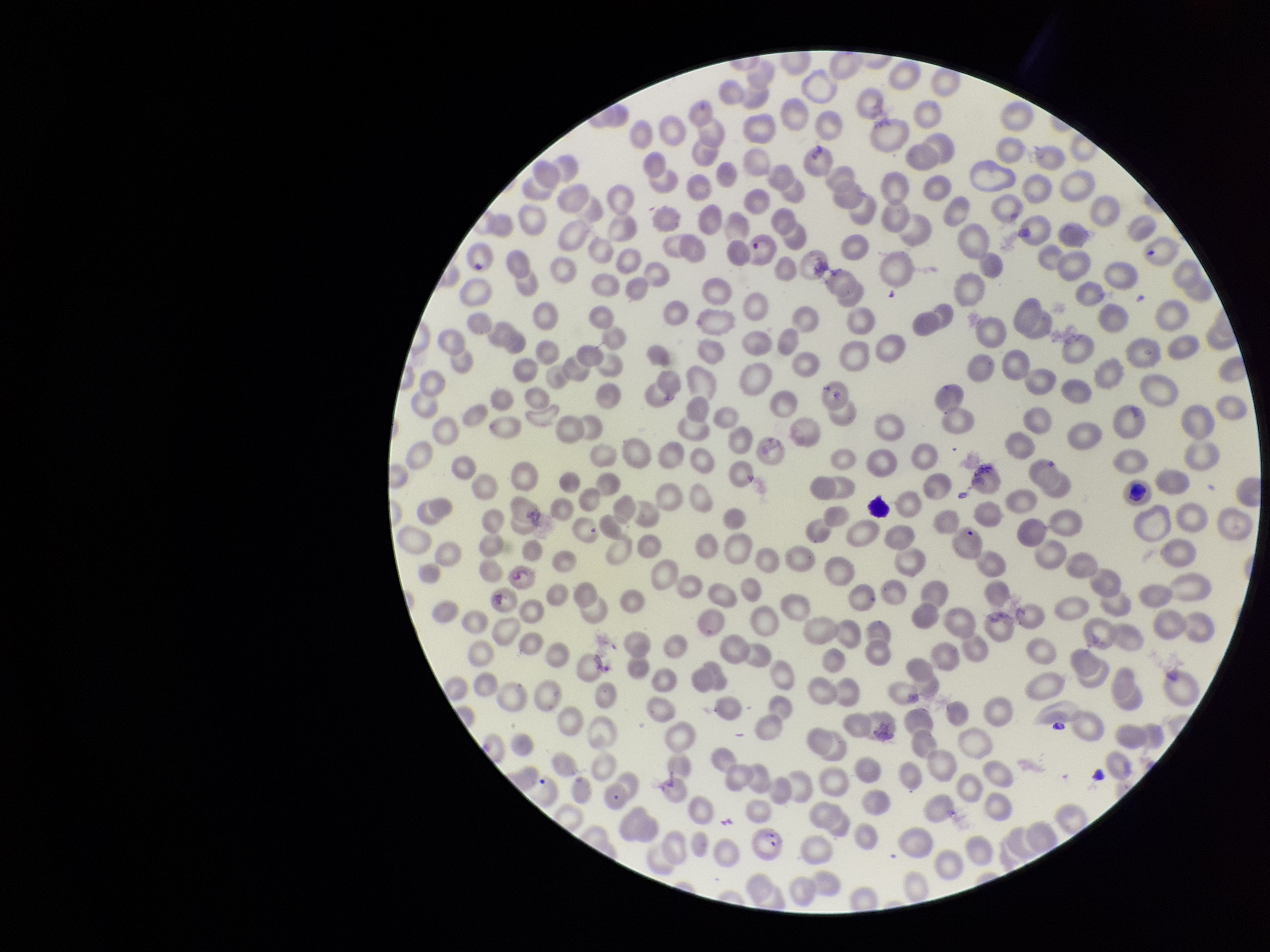
field of view = one from this slide
capture = smartphone photograph through the microscope eyepiece
image size = 1270×952 pixels
parasitized red blood cell count = 3
patient malaria status = positive
species reported for this patient = Plasmodium falciparum
preparation = thin blood smear
parasitized red blood cells = seen
stain = Giemsa
red blood cell count = 318